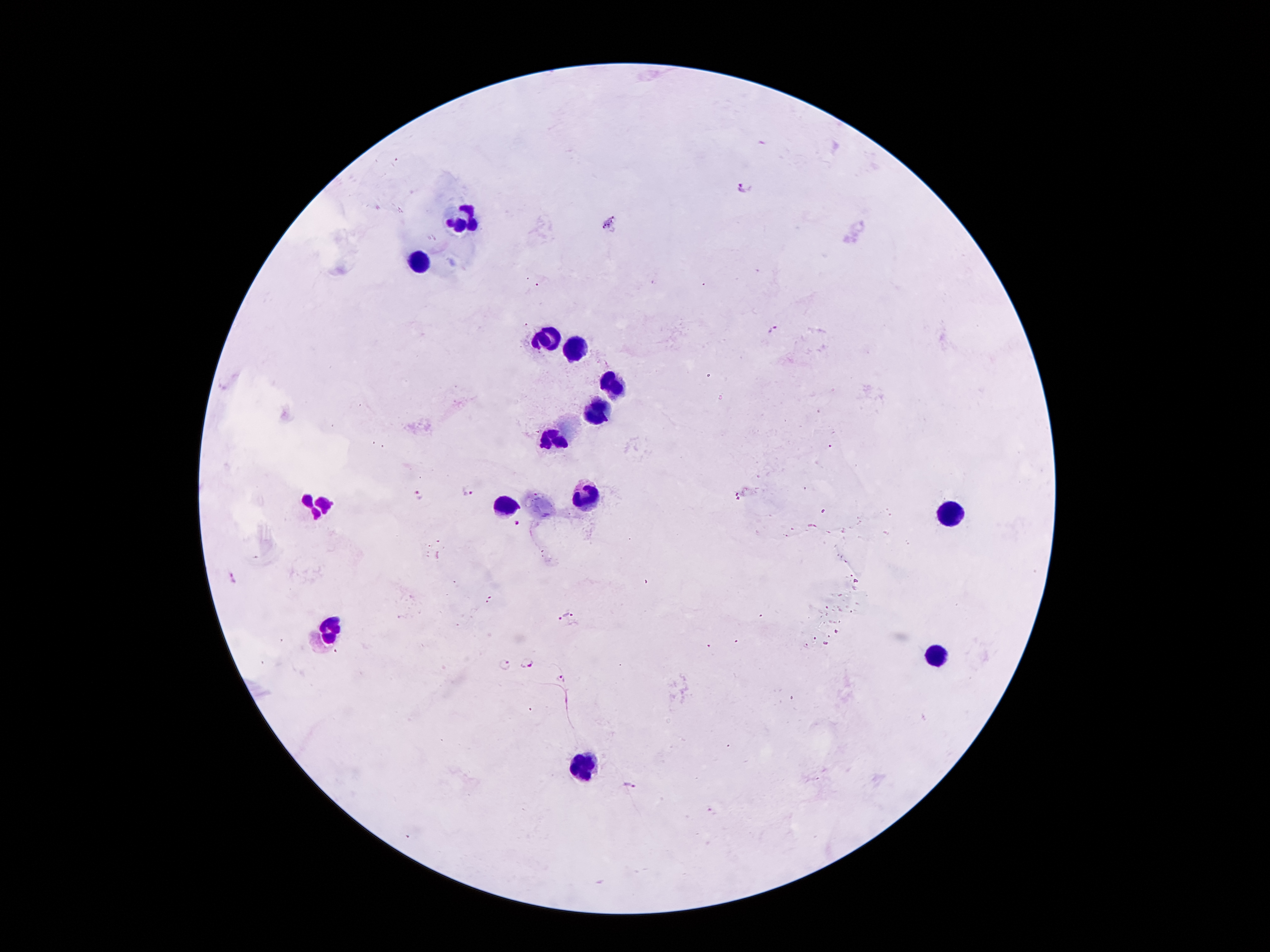
coordinate format = approximate centers as (x, y) in pixels
Plasmodium parasite locations = (745, 187), (773, 331), (468, 492), (419, 495), (517, 522), (234, 578), (564, 616), (528, 662), (505, 663), (561, 679), (631, 786)
leukocyte locations = (466, 218), (416, 263), (548, 336), (575, 347), (613, 384), (600, 410), (554, 439), (584, 494), (315, 500), (504, 506), (949, 513), (332, 628), (938, 655), (583, 769)
patient malaria status = positive for Plasmodium falciparum
preparation = thick blood smear
field of view = single
magnification = 100x
image size = 1270×952 pixels
capture = smartphone camera through the microscope eyepiece
stain = Giemsa